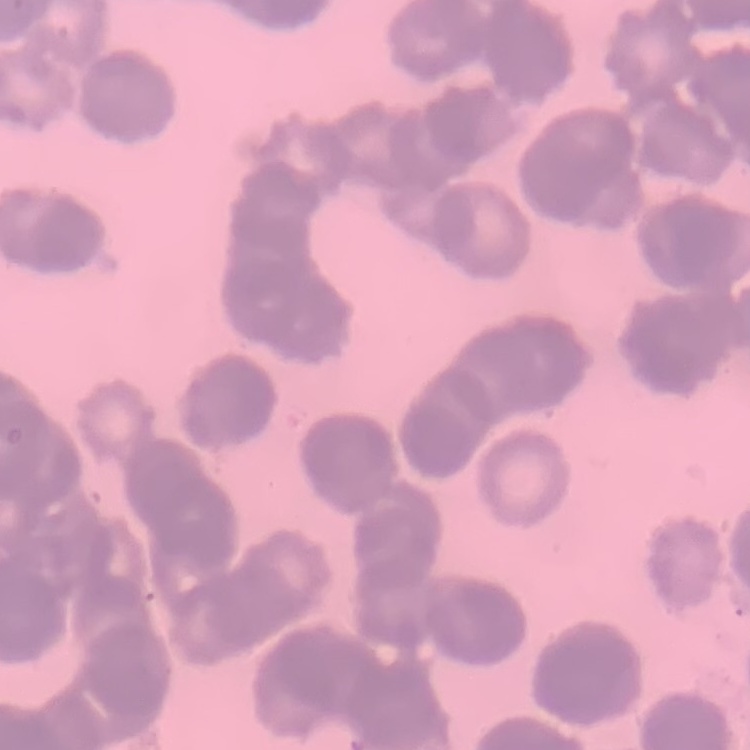
The red blood cells exhibit rouleaux formation. Thin peripheral smear. One tile cut from a larger photomicrograph. Stained with either Field's or Giemsa.